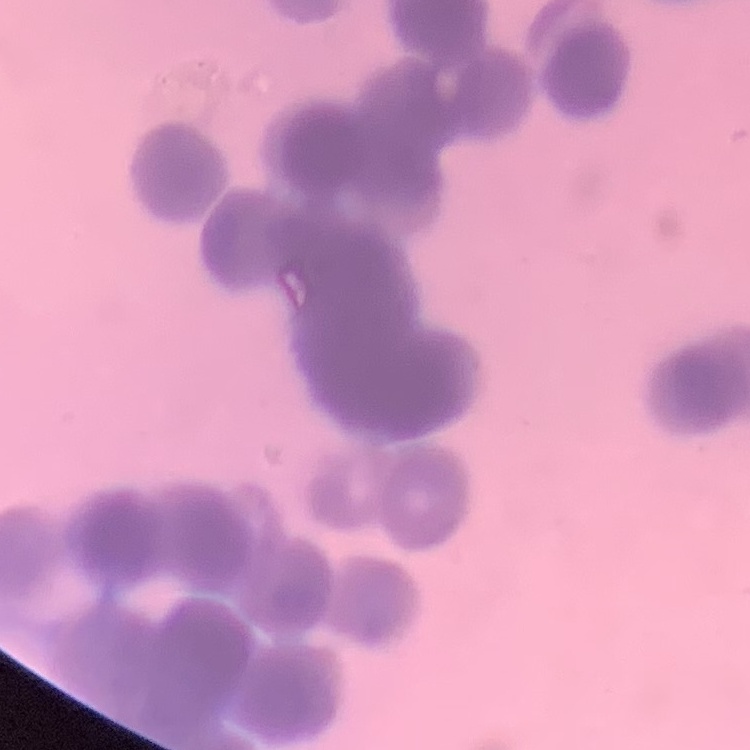
The erythrocytes show rouleaux formation. One tile cut from a larger photomicrograph. Thin blood smear. Field's or Giemsa stain.